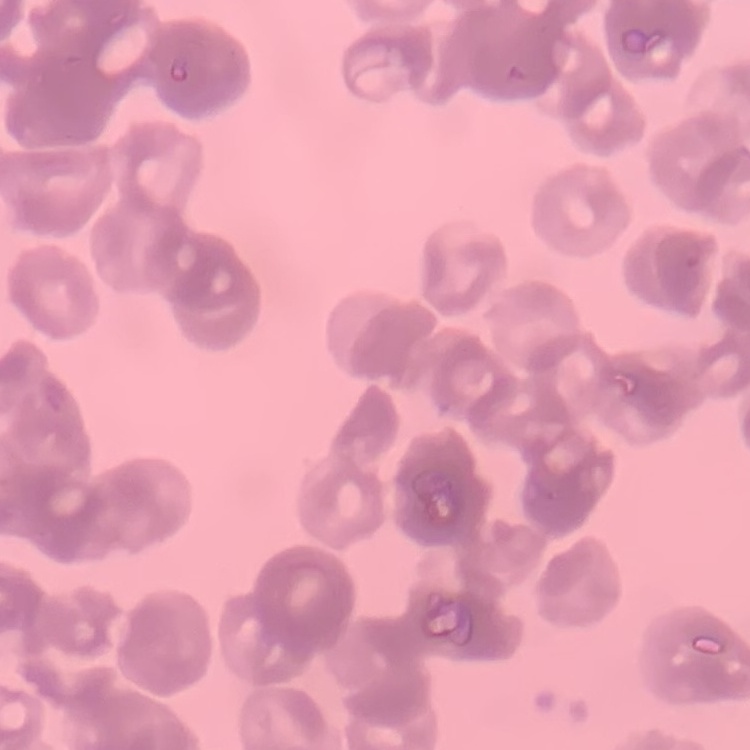

red blood cell morphology = rouleaux formation
image type = one tile cut from a larger photomicrograph
preparation = thin blood film
stain = Field's or Giemsa